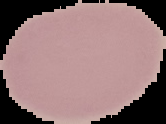
Summary:
  - Image size: 166×124 pixels
  - Preparation: thin blood smear
  - Image type: segmented cell region on a black background
  - Result: negative for malaria parasites